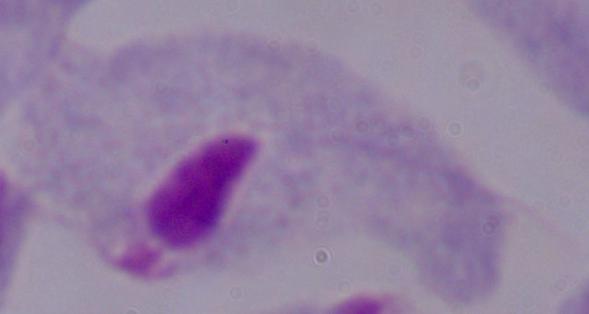 Micrograph. A trichomonad is shown. Captured at 1000x magnification.